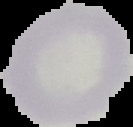

Malaria status: uninfected. From a thin blood smear. Image is 133×127 pixels. The area outside the segmented cell region is set to black.